Describe the morphology of the erythrocytes.
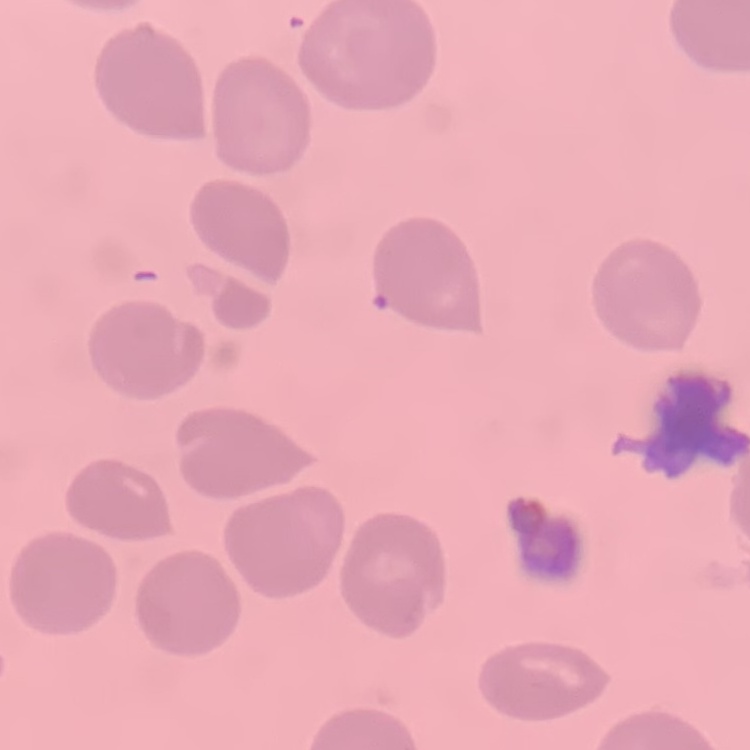

They show no rouleaux formation.

Square crop of a larger photomicrograph. Field's or Giemsa stain. Thin peripheral smear.